Identify the parasite.
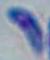

Toxoplasma gondii.

1000x magnification. Photomicrograph.